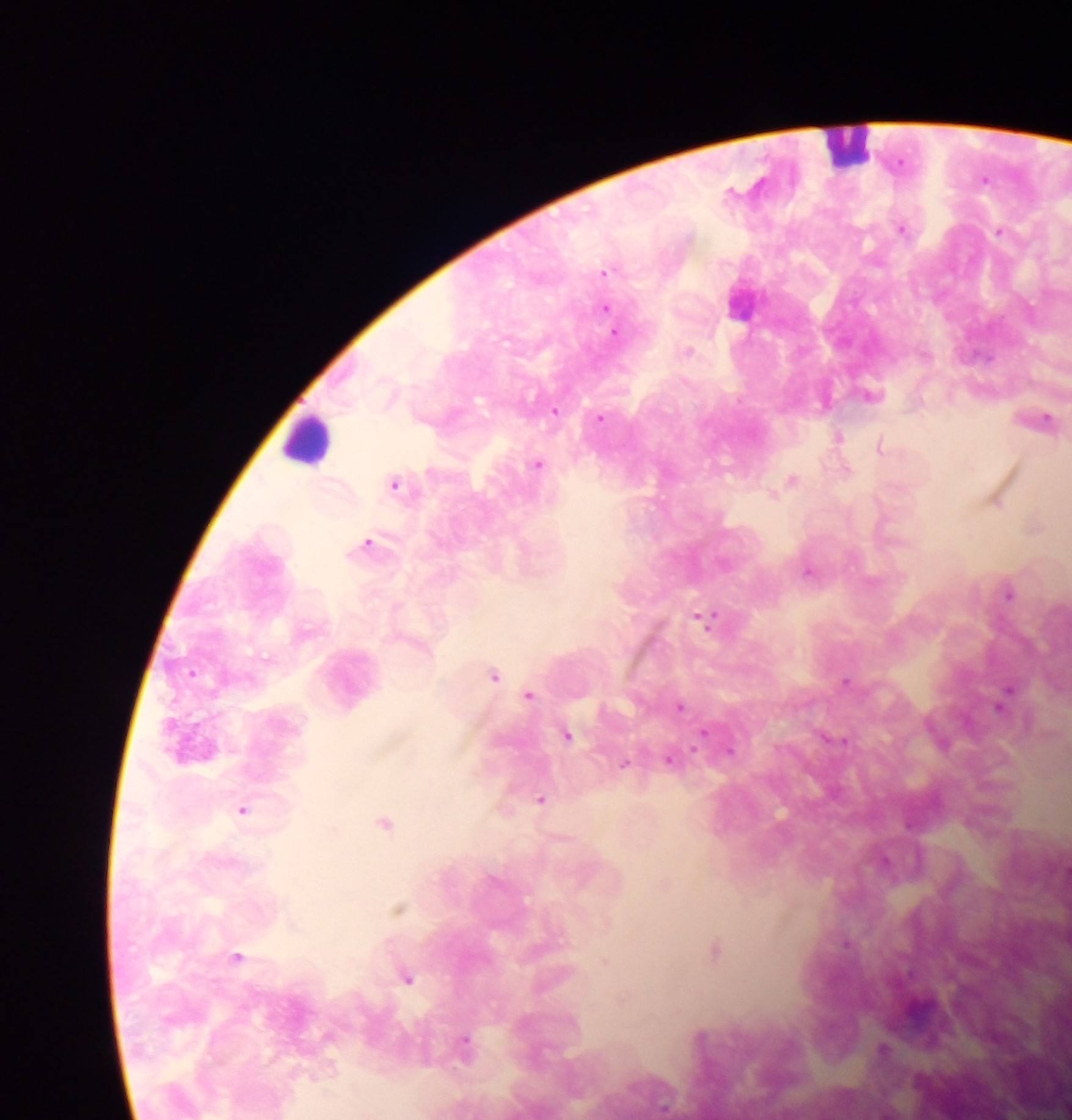 Approximate centers as (x, y) in pixels. Plasmodium parasite locations: (984, 178), (902, 228), (998, 231), (605, 271), (739, 301), (605, 307), (613, 332), (688, 350), (872, 394), (554, 410), (600, 418), (1045, 418), (838, 437), (879, 446), (537, 464), (846, 469), (792, 480), (395, 484), (996, 503), (368, 542), (809, 572), (1008, 594), (706, 619), (493, 675), (845, 681), (529, 695), (1005, 695), (680, 706), (702, 734), (568, 735), (837, 739), (730, 751), (670, 759), (625, 763), (541, 799), (242, 810), (384, 822), (398, 909), (714, 951), (237, 955), (408, 979), (465, 1041), (884, 1049). Leukocyte locations: (851, 144), (306, 439). Thick blood smear. Image is 1072×1120 pixels. Mobile-phone photograph taken through the microscope. Collected in Ghana. Single field of view.